State the blood parasite species.
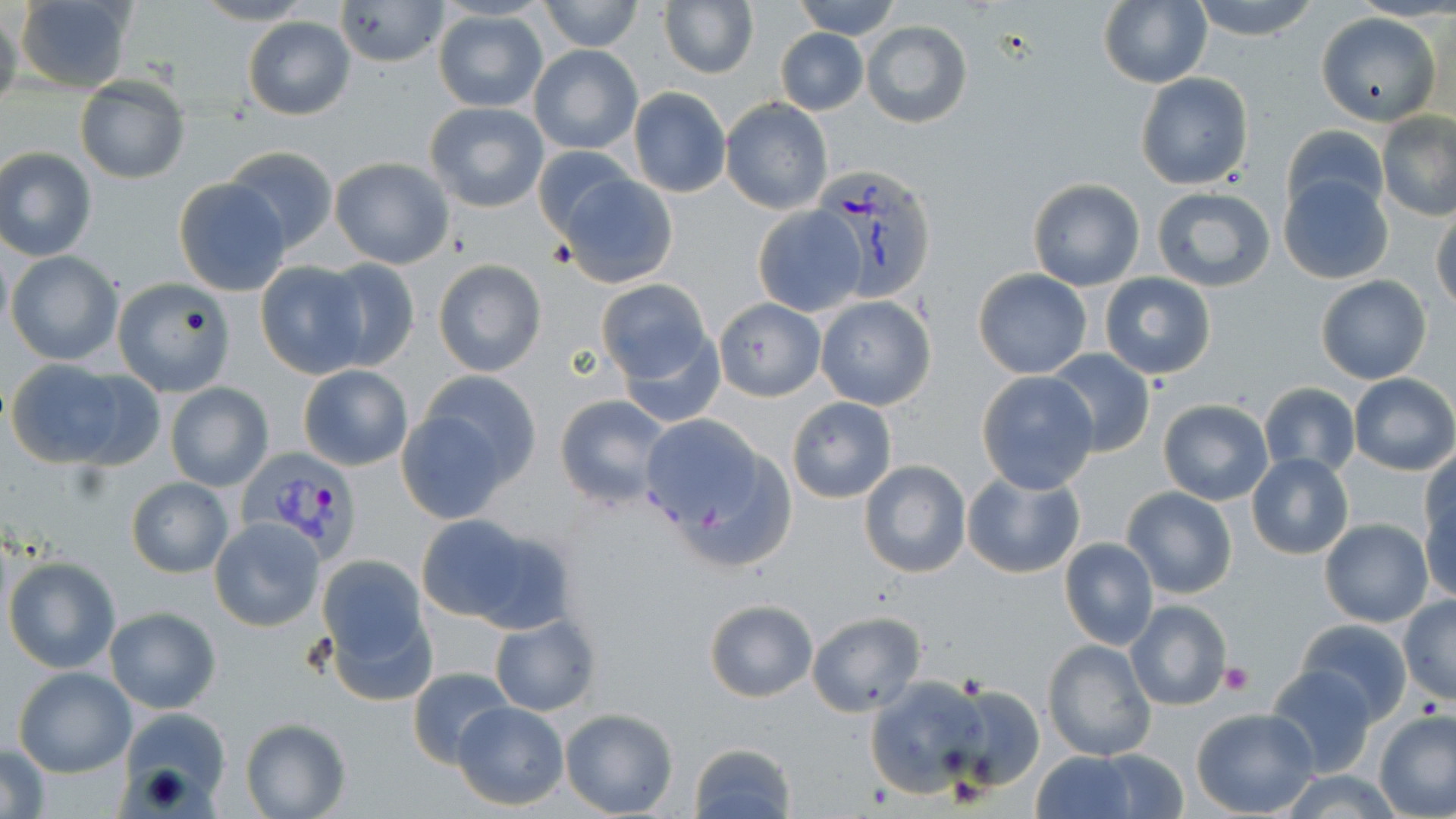

Plasmodium vivax.

Approximate bounding boxes as (x1, y1, x2, y2) in pixels. Plasmodium vivax-infected red blood cell locations: (809, 164, 937, 301), (236, 446, 362, 562). Platelet locations: (1218, 662, 1252, 694). Uninfected red blood cell locations: (15, 0, 137, 94), (191, 0, 317, 26), (334, 0, 449, 68), (658, 0, 758, 80), (789, 0, 902, 39), (1098, 0, 1213, 89), (1189, 0, 1322, 41), (537, 1, 644, 52), (0, 8, 22, 116), (433, 10, 548, 112), (1316, 11, 1440, 125), (243, 16, 355, 120), (861, 19, 972, 128), (775, 29, 867, 116), (529, 45, 643, 154), (1135, 72, 1254, 190), (75, 77, 190, 185), (628, 87, 731, 198), (722, 98, 832, 213), (424, 101, 549, 213), (1377, 112, 1456, 220), (1281, 125, 1389, 220), (533, 145, 638, 243), (222, 146, 338, 251), (0, 147, 97, 260), (329, 156, 455, 269), (1278, 171, 1394, 284), (557, 172, 680, 289), (172, 177, 292, 296), (1027, 177, 1145, 291), (1151, 187, 1275, 294), (751, 205, 867, 317), (1432, 206, 1456, 313), (6, 251, 123, 365), (319, 257, 420, 369), (433, 258, 547, 377), (254, 261, 370, 379), (971, 268, 1091, 379), (1100, 273, 1215, 380), (1315, 275, 1431, 384), (112, 276, 236, 396), (595, 279, 714, 388), (815, 295, 936, 410), (713, 298, 826, 401), (614, 322, 727, 427), (1045, 348, 1155, 458), (6, 359, 152, 469), (298, 364, 413, 471), (415, 369, 544, 494), (976, 371, 1101, 494), (1350, 374, 1456, 475), (165, 382, 274, 492), (1259, 383, 1360, 479), (554, 395, 675, 512), (786, 396, 897, 504), (1157, 398, 1273, 505), (394, 402, 519, 524), (635, 414, 781, 552), (1421, 450, 1455, 552), (1247, 453, 1354, 560), (858, 459, 972, 580), (961, 467, 1086, 579), (126, 477, 233, 577), (1421, 485, 1456, 600), (1122, 486, 1236, 600), (418, 512, 575, 635), (209, 518, 324, 631), (1320, 518, 1433, 626), (1059, 538, 1158, 650), (315, 554, 434, 687), (3, 557, 121, 673), (1398, 596, 1456, 705), (703, 598, 818, 703), (1125, 600, 1232, 711), (104, 608, 221, 713), (806, 611, 926, 716), (488, 613, 601, 715), (1295, 618, 1413, 723), (1042, 638, 1157, 763), (1266, 664, 1377, 779), (406, 667, 514, 767), (14, 668, 136, 777), (865, 674, 991, 800), (946, 685, 1045, 793), (451, 701, 569, 811), (1192, 707, 1320, 817), (114, 708, 228, 811), (560, 708, 679, 817), (1374, 711, 1456, 818), (241, 718, 351, 819), (689, 741, 796, 819), (1, 743, 52, 819), (1089, 750, 1189, 818), (1031, 751, 1139, 819), (1275, 769, 1402, 819). May-Grünwald-Giemsa-stained preparation. Image is 1456×819 pixels. 1000x magnification. Thin blood smear. Light microscopy. Single field of view.